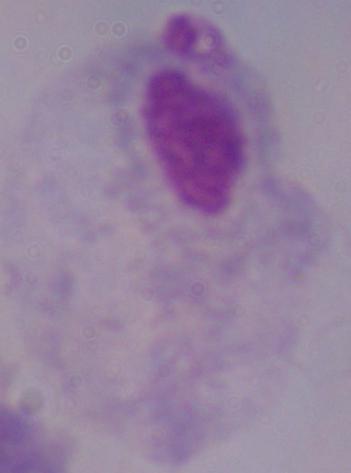
modality = micrograph
magnification = 1000x
identification = trichomonad